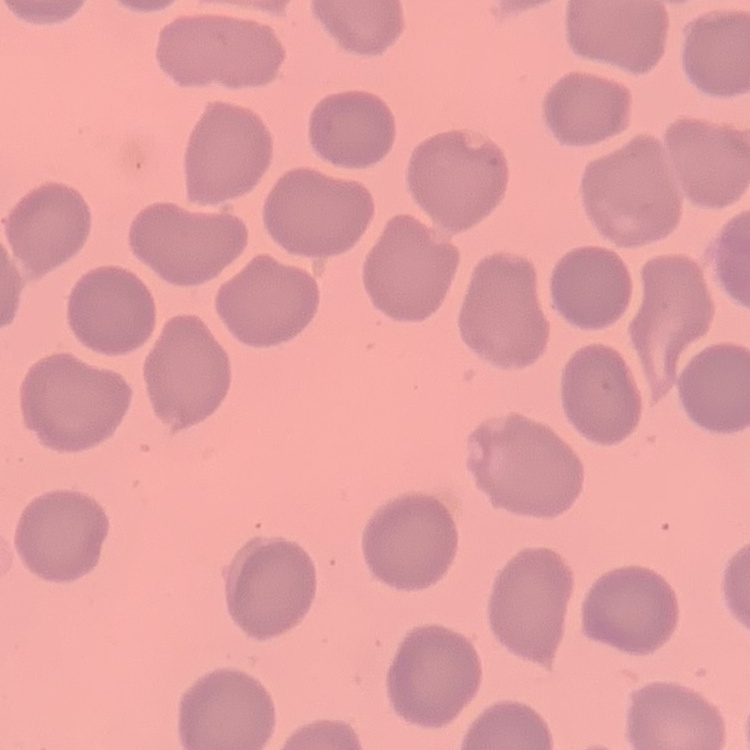

erythrocyte morphology = no rouleaux formation
stain = Field's or Giemsa
image type = one tile cut from a larger photomicrograph
preparation = thin blood smear